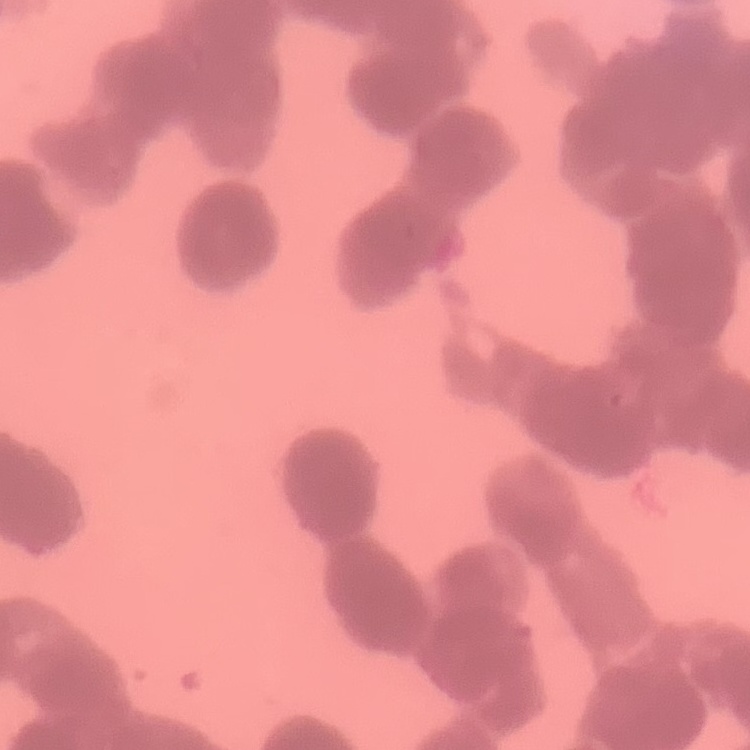
erythrocyte morphology = rouleaux formation
image type = square crop of a larger photomicrograph
preparation = thin blood film
stain = Field's or Giemsa